Locate and identify every blood parasite.
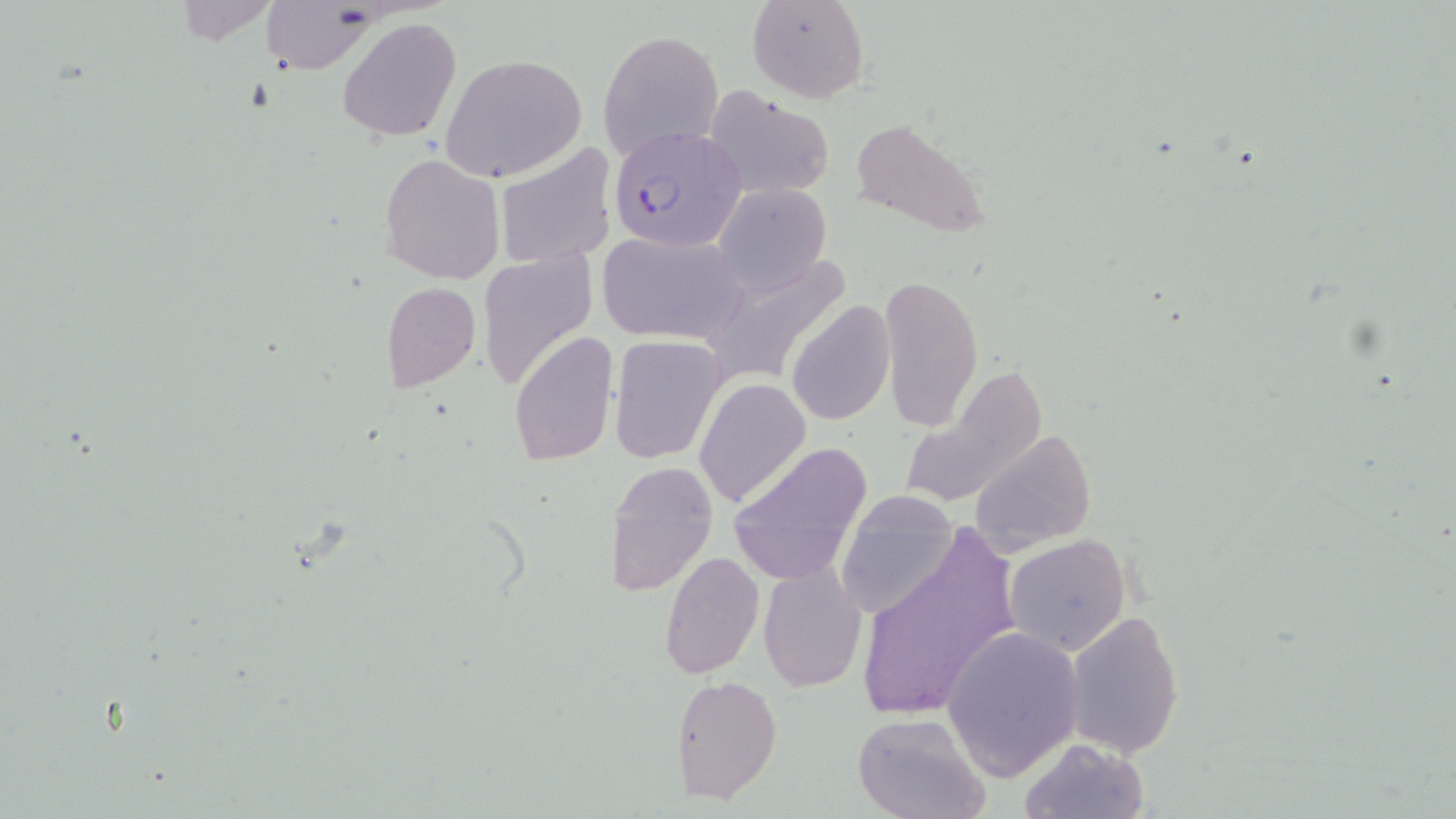
Approximate bounding boxes as (x1, y1, x2, y2) in pixels.
Plasmodium falciparum-infected red blood cells: (608, 126, 746, 252).
No Plasmodium ovale, Plasmodium malariae, Plasmodium vivax, Babesia divergens, or Trypanosoma brucei observed.

Uninfected red blood cell locations: (747, 0, 870, 103), (259, 3, 372, 72), (336, 16, 463, 143), (597, 27, 726, 161), (440, 53, 588, 182), (703, 88, 834, 198), (849, 116, 990, 238), (493, 144, 618, 269), (380, 154, 506, 284), (714, 183, 830, 294), (596, 231, 749, 344), (704, 248, 853, 377), (480, 250, 598, 393), (878, 275, 982, 430), (382, 282, 480, 394), (787, 299, 896, 426), (508, 330, 619, 468), (608, 334, 727, 462), (896, 364, 1046, 511), (696, 380, 811, 508), (973, 426, 1096, 549), (729, 442, 872, 584), (603, 462, 718, 595), (833, 489, 960, 622), (853, 526, 1023, 724), (1005, 535, 1132, 656), (659, 550, 764, 680), (757, 562, 867, 694), (1064, 608, 1185, 758), (940, 623, 1084, 784), (669, 674, 783, 805), (851, 711, 989, 819), (1017, 737, 1148, 819). Slide-level diagnosis: Plasmodium falciparum. Thin blood film. Single field of view. Optical microscopy. Image is 1456×819 pixels. May-Grünwald-Giemsa-stained preparation. 1000x magnification.